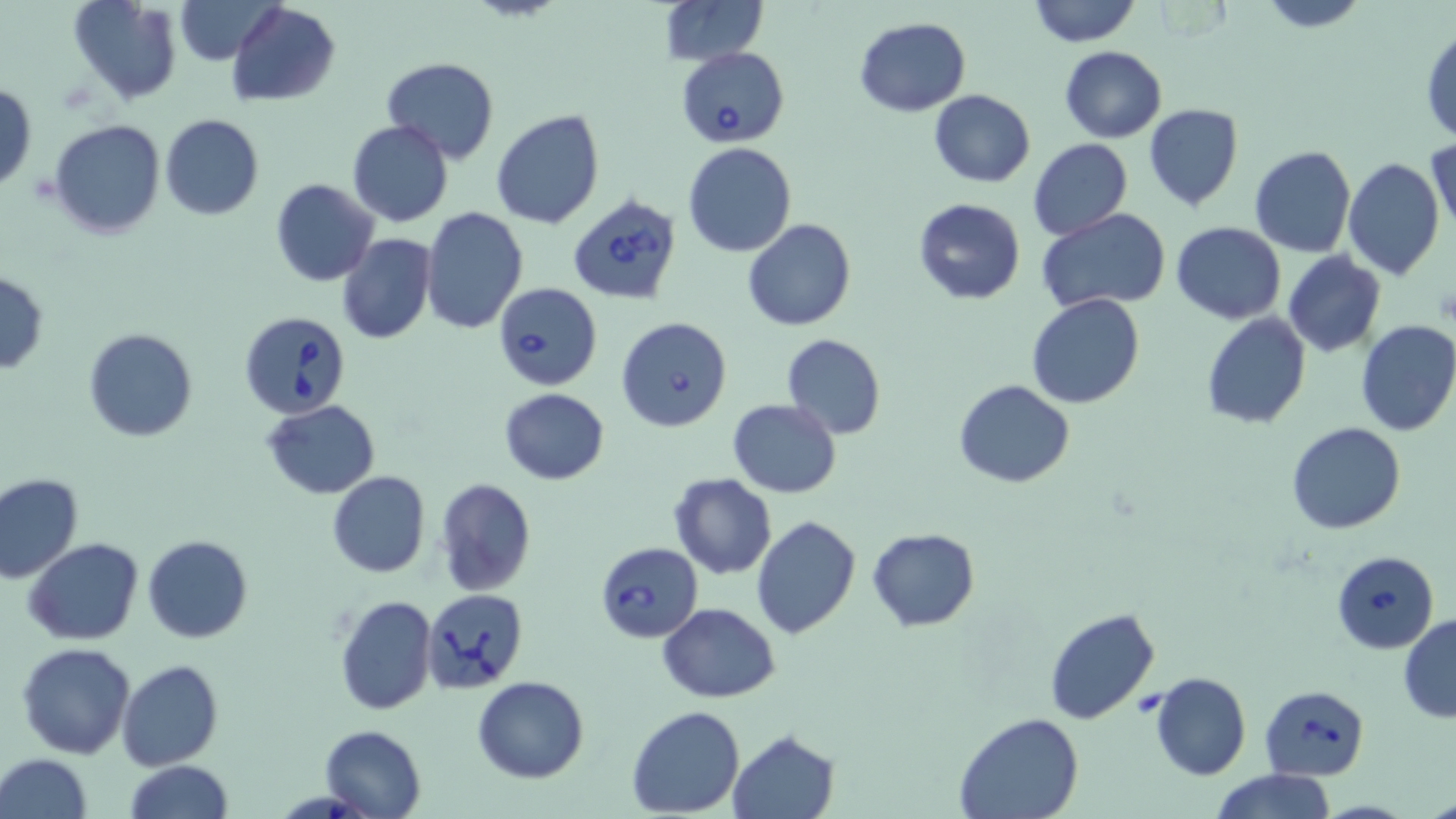
Babesia divergens-infected red blood cell locations = approximate bounding boxes as named x1/y1/x2/y2 corners in pixels: (x1=676, y1=46, x2=790, y2=147), (x1=567, y1=192, x2=683, y2=305), (x1=495, y1=282, x2=602, y2=390), (x1=239, y1=310, x2=354, y2=419), (x1=616, y1=317, x2=733, y2=432), (x1=595, y1=542, x2=703, y2=642), (x1=1330, y1=550, x2=1440, y2=653), (x1=424, y1=589, x2=528, y2=694), (x1=1261, y1=685, x2=1369, y2=780)
slide-level diagnosis = Babesia divergens
image size = 1456×819 pixels
modality = optical microscopy
field of view = one of a larger specimen
uninfected red blood cell locations = approximate bounding boxes as named x1/y1/x2/y2 corners in pixels: (x1=66, y1=0, x2=181, y2=105), (x1=175, y1=0, x2=280, y2=66), (x1=659, y1=0, x2=767, y2=66), (x1=1027, y1=0, x2=1141, y2=47), (x1=1257, y1=0, x2=1370, y2=31), (x1=226, y1=2, x2=341, y2=105), (x1=855, y1=17, x2=969, y2=116), (x1=1422, y1=27, x2=1456, y2=146), (x1=1059, y1=46, x2=1167, y2=143), (x1=382, y1=57, x2=499, y2=165), (x1=0, y1=82, x2=37, y2=193), (x1=928, y1=89, x2=1034, y2=186), (x1=1143, y1=104, x2=1243, y2=211), (x1=490, y1=108, x2=605, y2=229), (x1=160, y1=114, x2=264, y2=220), (x1=49, y1=119, x2=165, y2=239), (x1=347, y1=120, x2=454, y2=227), (x1=1027, y1=137, x2=1132, y2=240), (x1=1428, y1=138, x2=1456, y2=238), (x1=683, y1=142, x2=797, y2=256), (x1=1249, y1=144, x2=1356, y2=258), (x1=1343, y1=157, x2=1445, y2=281), (x1=271, y1=179, x2=378, y2=286), (x1=912, y1=197, x2=1026, y2=305), (x1=422, y1=205, x2=527, y2=333), (x1=1038, y1=209, x2=1171, y2=312), (x1=743, y1=219, x2=855, y2=331), (x1=1171, y1=221, x2=1286, y2=324), (x1=336, y1=233, x2=437, y2=345), (x1=1282, y1=252, x2=1385, y2=358), (x1=0, y1=269, x2=49, y2=375), (x1=1027, y1=293, x2=1145, y2=409), (x1=1200, y1=313, x2=1312, y2=429), (x1=1354, y1=319, x2=1456, y2=437), (x1=84, y1=328, x2=197, y2=442), (x1=781, y1=334, x2=886, y2=440), (x1=954, y1=379, x2=1076, y2=488), (x1=499, y1=388, x2=610, y2=484), (x1=262, y1=399, x2=381, y2=500), (x1=727, y1=399, x2=842, y2=497), (x1=1285, y1=422, x2=1406, y2=535), (x1=326, y1=471, x2=430, y2=578), (x1=0, y1=472, x2=84, y2=584), (x1=670, y1=473, x2=776, y2=579), (x1=434, y1=477, x2=535, y2=598), (x1=751, y1=517, x2=861, y2=639), (x1=866, y1=527, x2=981, y2=633), (x1=142, y1=536, x2=253, y2=642), (x1=24, y1=538, x2=144, y2=645), (x1=335, y1=592, x2=437, y2=715), (x1=659, y1=602, x2=780, y2=704), (x1=1044, y1=607, x2=1161, y2=725), (x1=1398, y1=614, x2=1456, y2=723), (x1=16, y1=643, x2=136, y2=759), (x1=117, y1=660, x2=223, y2=770), (x1=1151, y1=672, x2=1251, y2=779), (x1=472, y1=676, x2=590, y2=784), (x1=4, y1=700, x2=109, y2=816), (x1=627, y1=705, x2=745, y2=817), (x1=954, y1=713, x2=1083, y2=819), (x1=319, y1=724, x2=427, y2=819), (x1=727, y1=728, x2=839, y2=818), (x1=1, y1=754, x2=93, y2=819), (x1=125, y1=760, x2=234, y2=819), (x1=1210, y1=768, x2=1336, y2=819), (x1=1425, y1=789, x2=1456, y2=819)
magnification = 1000x
preparation = thin blood film
stain = May-Grünwald-Giemsa